Report the malaria status of this cell.
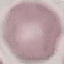

It is uninfected.

Giemsa stain. Automatically extracted cell patch, resized to 64 × 64 pixels. Photographed with a smartphone camera at the microscope eyepiece. Thin blood smear.